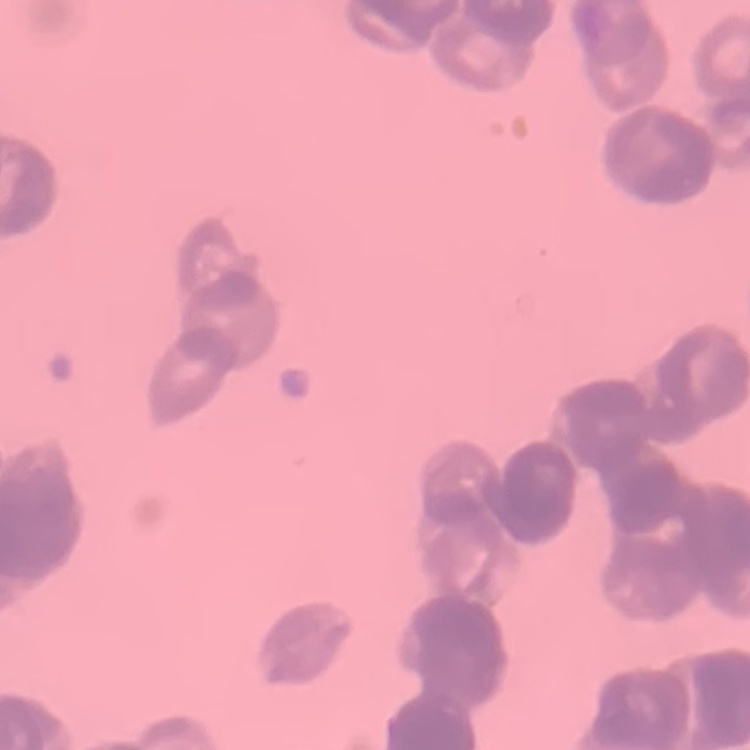 The erythrocytes show rouleaux formation. Square crop of a larger photomicrograph. Thin blood smear. Stained with either Field's or Giemsa.